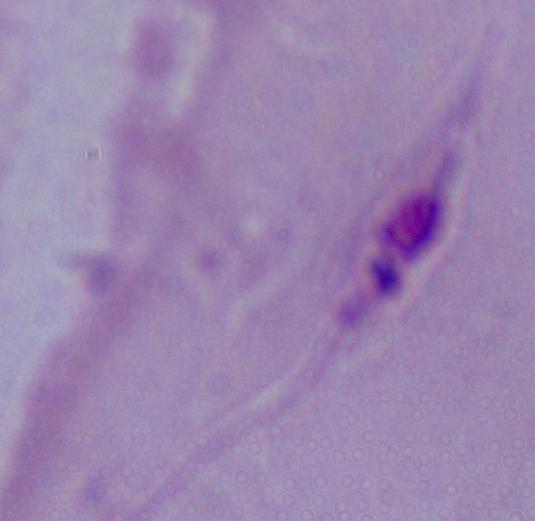
Summary:
  - Identification: Leishmania
  - Magnification: 1000x
  - Modality: photomicrograph